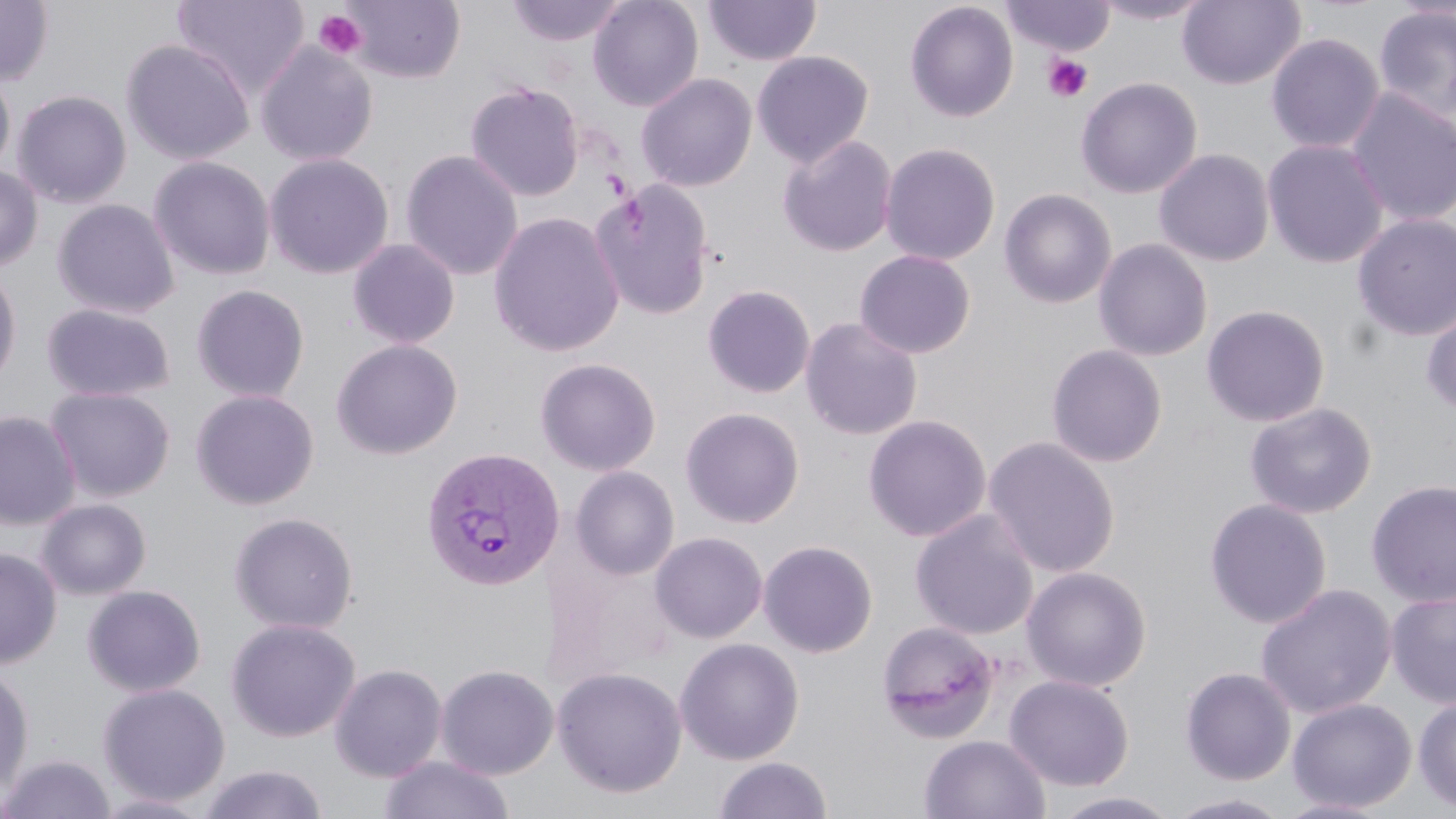
Approximate bounding boxes as (x1, y1, x2, y2) in pixels. Platelet locations: (312, 9, 368, 61), (1043, 54, 1093, 102). Uninfected red blood cell locations: (0, 0, 54, 86), (171, 0, 310, 99), (340, 0, 466, 84), (505, 0, 627, 47), (587, 0, 704, 112), (703, 0, 821, 67), (1001, 0, 1115, 57), (1092, 0, 1212, 24), (1177, 0, 1306, 90), (904, 1, 1019, 123), (1373, 5, 1456, 124), (1265, 32, 1384, 154), (120, 38, 255, 165), (255, 41, 379, 167), (751, 50, 874, 167), (0, 68, 16, 179), (635, 73, 758, 192), (1076, 76, 1203, 199), (465, 80, 585, 202), (1345, 87, 1456, 228), (11, 90, 132, 208), (777, 134, 898, 257), (1262, 139, 1390, 269), (880, 142, 1001, 265), (1153, 148, 1275, 266), (400, 149, 523, 281), (264, 152, 394, 280), (148, 156, 276, 281), (0, 164, 43, 272), (591, 179, 715, 321), (998, 188, 1118, 309), (52, 198, 180, 320), (489, 211, 625, 358), (1352, 212, 1456, 343), (347, 238, 460, 349), (1093, 238, 1213, 362), (854, 249, 976, 359), (0, 262, 22, 390), (191, 284, 310, 402), (702, 284, 816, 399), (42, 303, 176, 403), (1201, 304, 1330, 427), (1421, 305, 1456, 415), (800, 316, 923, 440), (331, 338, 463, 460), (1046, 344, 1168, 467), (535, 357, 661, 476), (46, 386, 175, 502), (190, 388, 319, 510), (1244, 401, 1377, 519), (679, 406, 804, 528), (0, 410, 80, 530), (863, 414, 991, 543), (983, 435, 1120, 579), (570, 466, 680, 580), (1366, 479, 1456, 608), (37, 498, 151, 600), (1204, 498, 1332, 629), (910, 508, 1040, 640), (229, 511, 359, 634), (649, 531, 768, 643), (758, 539, 878, 657), (0, 548, 61, 668), (547, 550, 678, 685), (1021, 565, 1151, 692), (1255, 582, 1396, 719), (83, 584, 206, 697), (1385, 589, 1456, 708), (225, 617, 361, 742), (876, 619, 1001, 743), (674, 637, 804, 765), (0, 662, 34, 799), (329, 663, 448, 782), (435, 663, 559, 780), (551, 665, 688, 799), (1180, 666, 1296, 785), (1004, 674, 1134, 791), (98, 682, 230, 808), (1413, 695, 1456, 813), (1287, 698, 1417, 813), (919, 734, 1050, 819), (379, 754, 515, 819), (2, 755, 116, 818), (713, 756, 832, 818), (196, 764, 329, 819), (1050, 791, 1183, 818), (93, 793, 213, 818), (1166, 793, 1294, 819), (1276, 797, 1393, 819). Plasmodium vivax-infected red blood cell locations: (421, 446, 565, 591). Slide-level diagnosis: Plasmodium vivax. Thin blood film. One field of a larger specimen. May-Grünwald-Giemsa stain. Image is 1456×819 pixels. Captured at 1000x magnification. Optical microscopy.